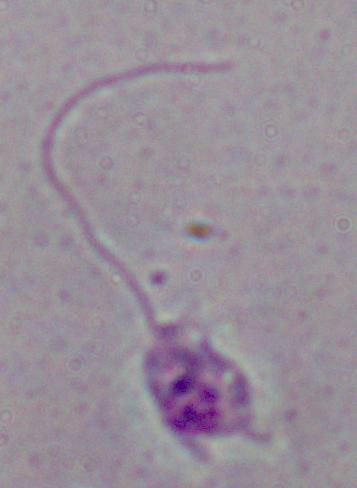
Summary:
  - Magnification: 1000x
  - Identification: Leishmania
  - Modality: photomicrograph